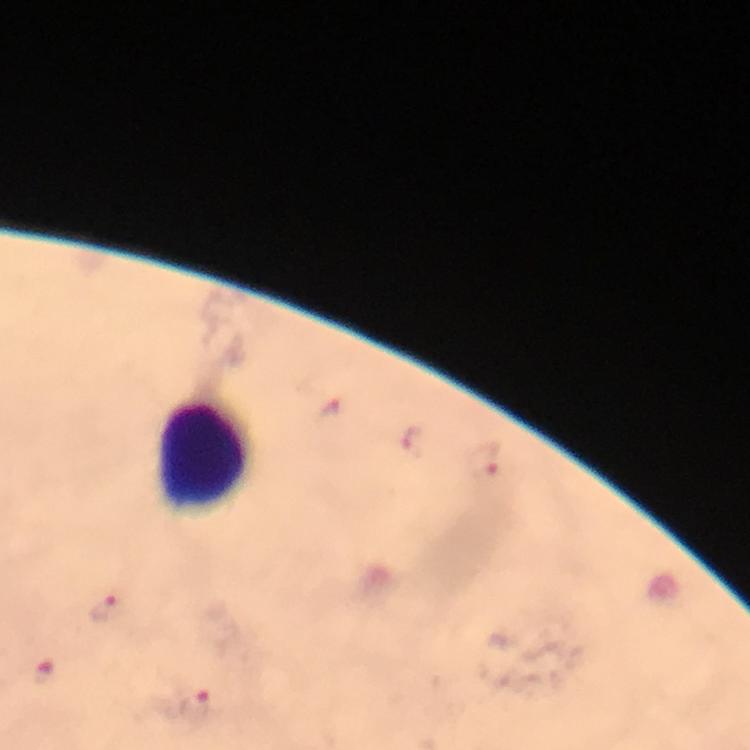

leukocyte locations = approximate centers as [x, y] in pixels: [205, 457]
image size = 750×750 pixels
immersion oil = used
context = from a malaria diagnostic workup
cropped from = one field of view
preparation = thick blood film
capture = smartphone photograph through a microscope
magnification = 100x
Plasmodium parasite locations = approximate centers as [x, y] in pixels: [332, 407], [411, 437], [483, 460], [103, 608], [44, 673], [196, 707]
stain = Giemsa